Classify this cell by malaria status.
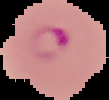
Parasitized.

image type = segmented cell region with the area outside set to black
preparation = thin blood smear
image size = 109×100 pixels